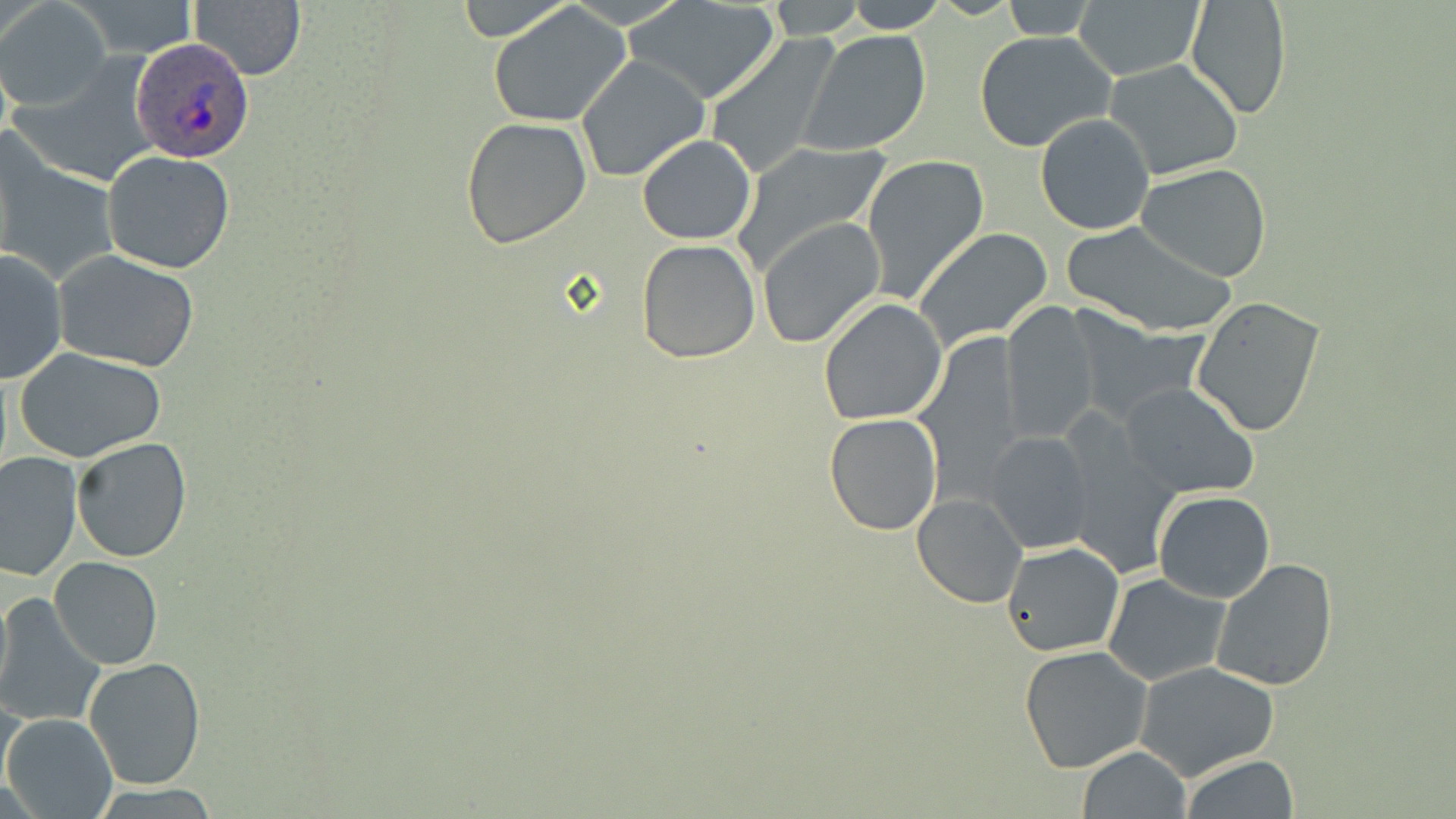
slide-level diagnosis = Plasmodium ovale
uninfected red blood cell locations = approximate bounding boxes as (x1,y1)-(x2,y2) corner pairs in pixels: (69,0)-(202,57), (187,0)-(306,80), (454,0)-(574,45), (842,0)-(947,32), (997,0)-(1100,38), (1184,0)-(1293,122), (2,1)-(110,109), (765,1)-(867,39), (629,2)-(780,105), (1074,2)-(1203,80), (487,3)-(631,128), (803,30)-(932,155), (975,31)-(1114,152), (703,32)-(844,181), (575,53)-(711,184), (1104,57)-(1244,180), (1035,113)-(1156,235), (461,116)-(593,250), (636,135)-(758,244), (730,138)-(892,276), (2,150)-(117,283), (102,151)-(235,275), (860,153)-(989,302), (1136,164)-(1273,282), (757,219)-(886,347), (1061,221)-(1237,336), (913,227)-(1055,352), (637,239)-(761,363), (0,249)-(68,385), (54,252)-(200,372), (1190,296)-(1328,436), (818,299)-(946,424), (1000,302)-(1103,442), (911,338)-(1027,506), (13,347)-(167,463), (1120,382)-(1260,499), (825,414)-(942,535), (986,431)-(1095,553), (1059,431)-(1180,578), (71,436)-(192,563), (0,451)-(82,583), (1154,491)-(1274,603), (912,493)-(1028,608), (1002,541)-(1125,657), (1209,556)-(1339,690), (50,558)-(162,669), (1103,572)-(1230,686), (0,584)-(13,704), (0,595)-(104,725), (1018,646)-(1154,774), (82,657)-(207,792), (1135,662)-(1281,782), (1,689)-(24,798), (4,712)-(117,819), (1078,746)-(1192,818), (1181,755)-(1299,819)
magnification = 1000x
Plasmodium ovale-infected red blood cell locations = approximate bounding boxes as (x1,y1)-(x2,y2) corner pairs in pixels: (132,41)-(257,163)
stain = May-Grünwald-Giemsa
image size = 1456×819 pixels
field of view = single
preparation = thin blood film
modality = optical microscopy